State the preparation type.
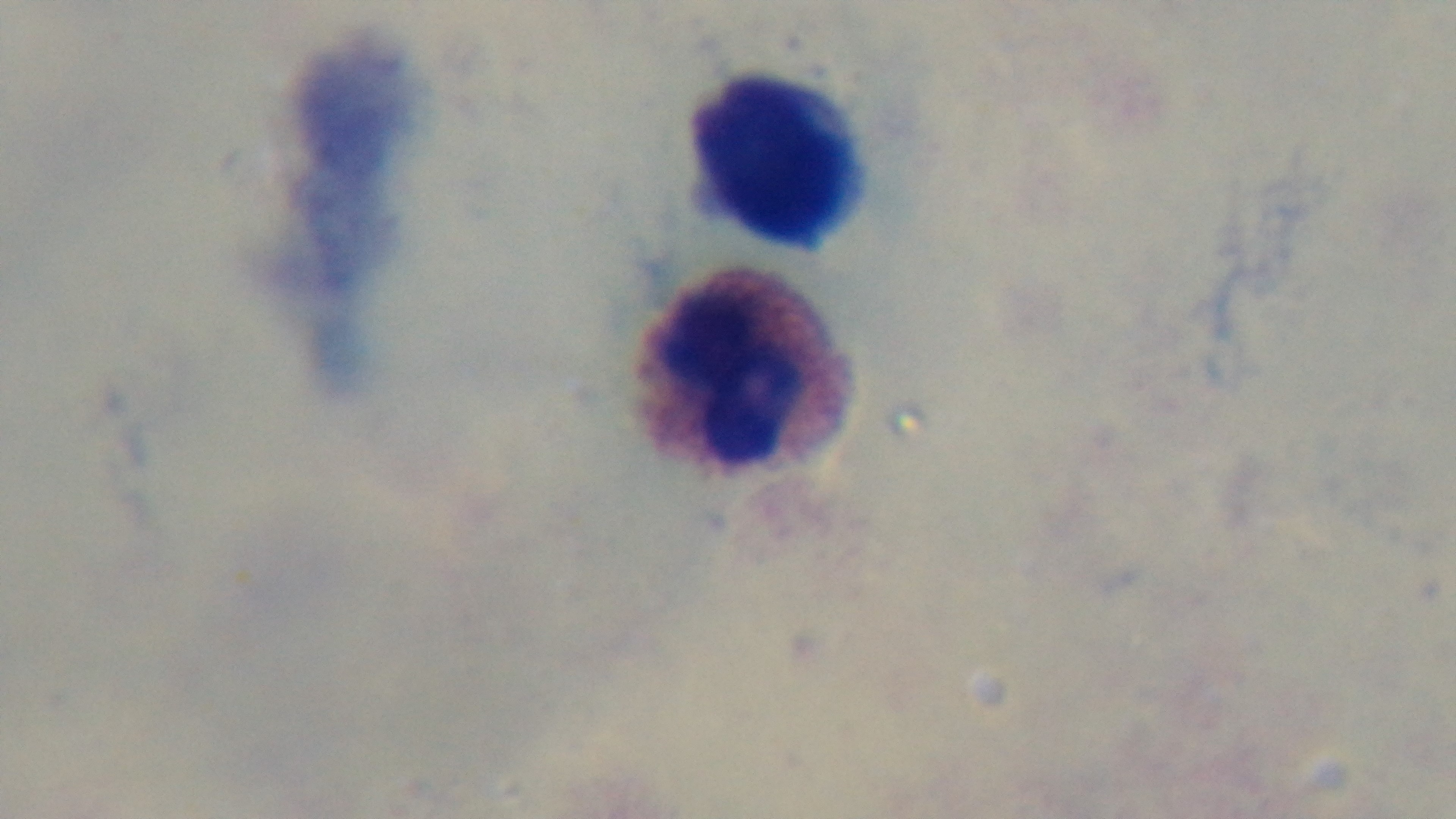

It is a thick blood film.

Summary:
  - Malaria status: uninfected
  - Field of view: single
  - Modality: light microscopy
  - Capture: mounted 4K digital camera
  - Objective: 100x oil immersion
  - Stain: Giemsa